Report the malaria status of this cell.
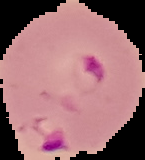

It is parasitized.

Summary:
  - Image size: 145×160 pixels
  - Image type: segmented cell region with the area outside set to black
  - Preparation: thin blood film